Report the malaria status of this cell.
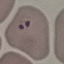

It is parasitized.

{
  "image_type": "cell patch, automatically extracted from a larger field of view and resized to 64 × 64 pixels",
  "stain": "Giemsa",
  "preparation": "thin smear",
  "capture": "smartphone camera at the microscope eyepiece"
}